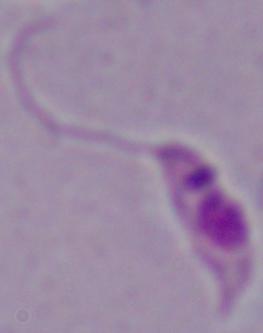

Summary:
  - Modality: micrograph
  - Identification: Leishmania
  - Magnification: 1000x